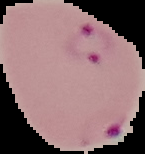
image type = segmented cell region on a black background
result = malaria parasites detected
image size = 145×154 pixels
preparation = thin blood smear